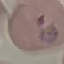

Summary:
  - Result: malaria parasites detected
  - Capture: smartphone camera at the microscope eyepiece
  - Image type: cell patch, automatically extracted from a larger field of view and resized to 64 × 64 pixels
  - Stain: Giemsa
  - Preparation: thin blood film